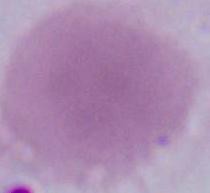
Summary:
  - Magnification: 1000x
  - Identification: red blood cell
  - Modality: micrograph